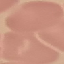

Summary:
  - Malaria status: uninfected
  - Capture: smartphone camera at the microscope eyepiece
  - Preparation: thin blood film
  - Image type: automatically extracted cell patch, resized to 64 × 64 pixels
  - Stain: Giemsa